Report the malaria status of this cell.
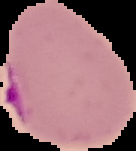

It is parasitized.

From a thin blood film. Image is 136×151 pixels. Cell region segmented out of the field of view; the surrounding area is masked to black.